State the blood parasite species.
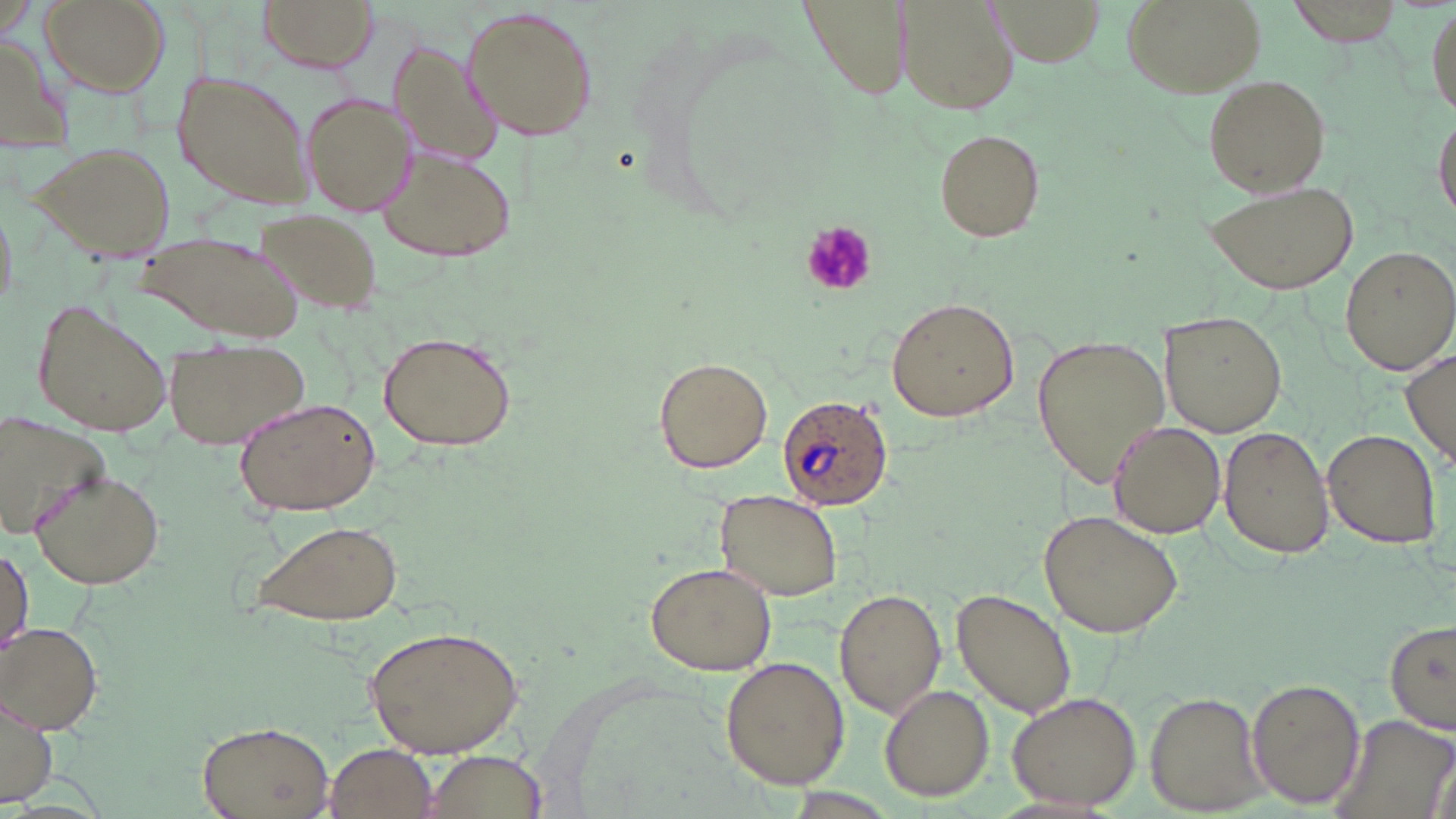

Plasmodium ovale.

Approximate bounding boxes as [x1, y1, x2, y2] in pixels. Uninfected red blood cell locations: [39, 0, 170, 96], [258, 0, 378, 72], [801, 0, 908, 100], [996, 0, 1100, 64], [1122, 0, 1264, 98], [1288, 0, 1405, 47], [900, 1, 1012, 114], [461, 5, 601, 144], [0, 32, 71, 152], [388, 36, 505, 171], [173, 69, 314, 208], [1202, 72, 1330, 197], [301, 92, 412, 216], [1432, 107, 1456, 228], [934, 128, 1045, 241], [33, 141, 177, 260], [379, 147, 517, 261], [1207, 179, 1360, 295], [254, 207, 383, 317], [138, 231, 307, 341], [1340, 243, 1453, 374], [30, 297, 172, 439], [886, 297, 1020, 423], [1161, 312, 1286, 436], [377, 330, 516, 453], [1031, 331, 1171, 486], [167, 338, 310, 451], [1400, 349, 1456, 465], [654, 356, 774, 473], [233, 396, 381, 516], [0, 409, 105, 536], [1106, 421, 1225, 538], [1219, 426, 1336, 559], [1322, 428, 1441, 547], [31, 467, 165, 589], [715, 490, 841, 601], [1039, 509, 1184, 639], [251, 518, 406, 628], [0, 544, 34, 659], [646, 560, 777, 675], [834, 587, 944, 719], [952, 589, 1076, 718], [1385, 618, 1456, 736], [0, 622, 102, 733], [366, 622, 525, 759], [720, 655, 849, 791], [1246, 677, 1365, 810], [880, 684, 995, 802], [1008, 690, 1142, 810], [1145, 691, 1268, 812], [1, 693, 59, 807], [1330, 710, 1456, 819], [195, 719, 335, 819], [323, 742, 438, 818], [416, 750, 552, 818]. Plasmodium ovale-infected red blood cell locations: [775, 396, 894, 511]. Platelet locations: [800, 221, 877, 297]. May-Grünwald-Giemsa-stained preparation. Single field of view. Light microscopy. 1000x magnification. Image is 1456×819 pixels. Thin blood smear.